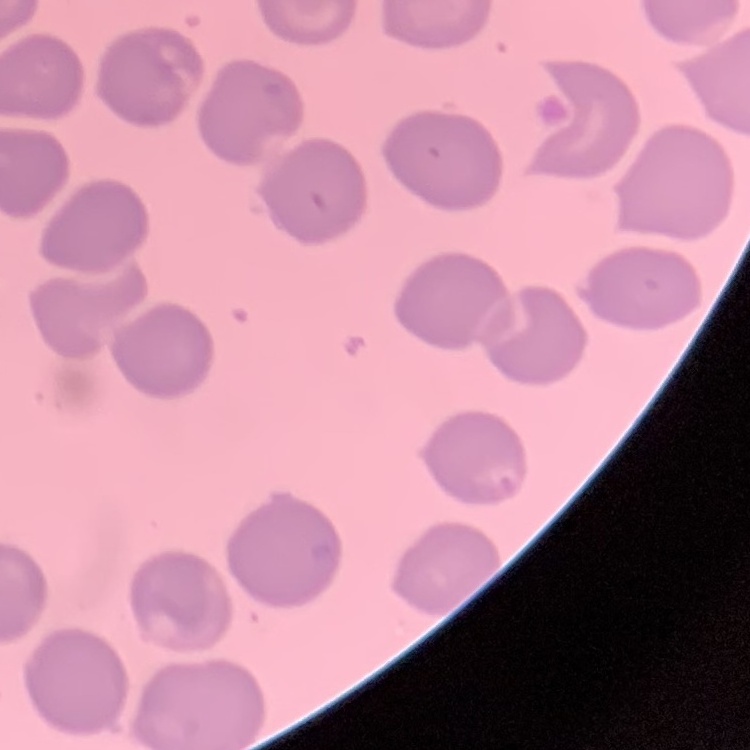
Summary:
  - Erythrocyte morphology: no rouleaux formation
  - Stain: Field's or Giemsa
  - Image type: square crop of a larger photomicrograph
  - Preparation: thin peripheral smear